Mark where leukocytes are.
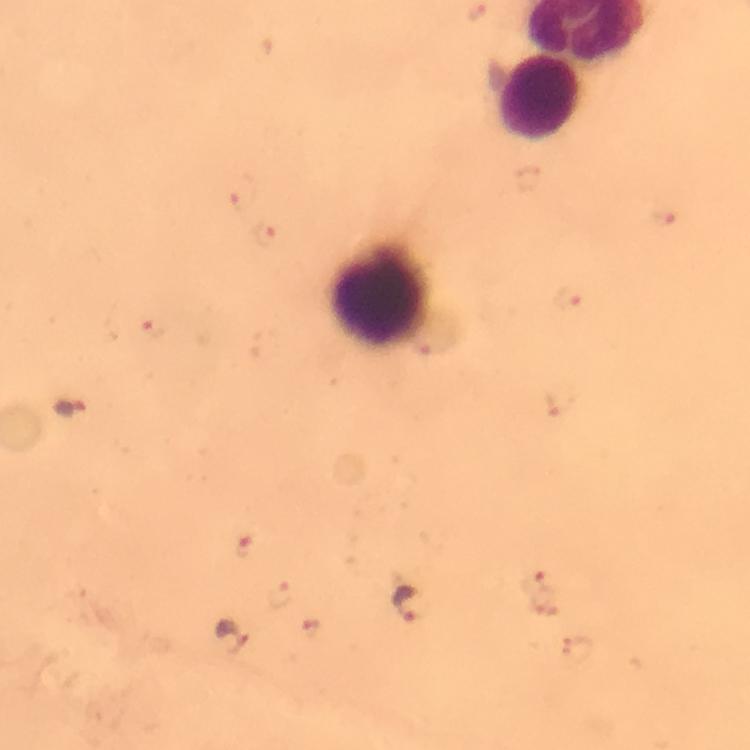

Approximate centers as [x, y] in pixels.
Leukocytes: [538, 97], [379, 296].

stain = Giemsa
image size = 750×750 pixels
context = from a malaria diagnostic workup
magnification = 100x
malaria parasite locations = approximate centers as [x, y] in pixels: [243, 193], [666, 217], [267, 233], [568, 296], [153, 330], [562, 401], [71, 408], [250, 544], [536, 582], [281, 596], [413, 605], [309, 631], [232, 639], [578, 649]
immersion oil = used
capture = smartphone camera through the microscope
cropped from = a single field of view
preparation = thick blood smear